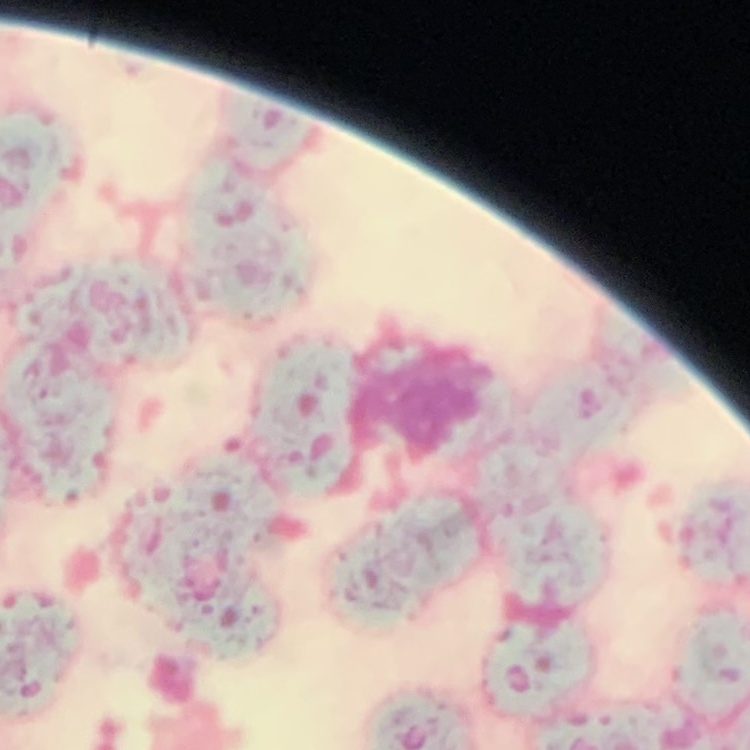
The red blood cells exhibit rouleaux formation. Thin peripheral smear. Square crop of a larger photomicrograph. Stained with either Field's or Giemsa.